Name the parasite shown.
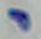

Toxoplasma gondii.

magnification = 1000x
modality = micrograph